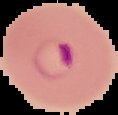

Summary:
  - Preparation: thin blood smear
  - Image size: 118×115 pixels
  - Malaria status: parasitized
  - Image type: segmented cell region on a black background